Report the malaria status of this cell.
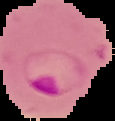

Parasitized.

image_size: 115×121 pixels
preparation: thin blood film
image_type: segmented cell region on a black background